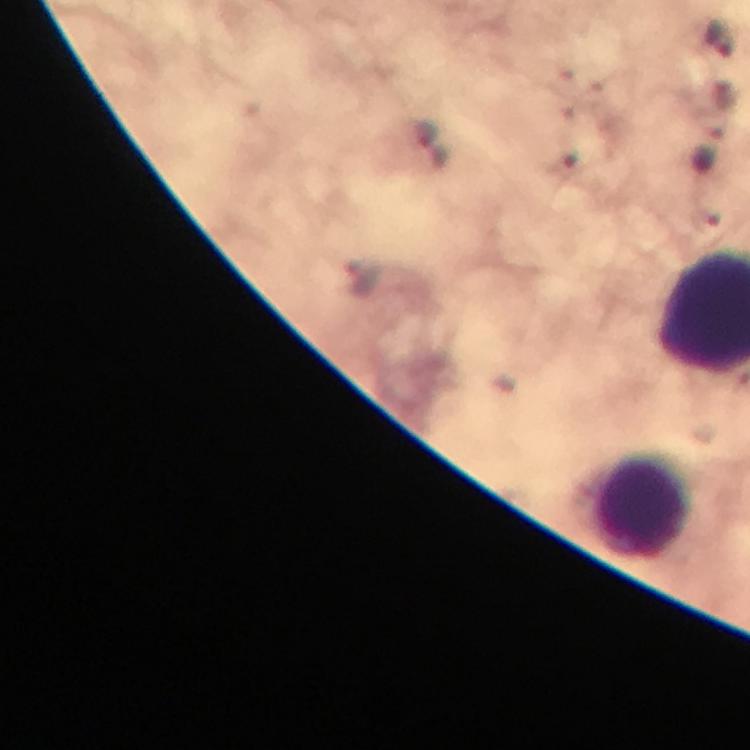

Approximate object centers, in pixels from the top-left corner.
Summary:
  - Plasmodium parasite locations: (x=434, y=147)
  - Leukocyte locations: (x=640, y=508)
  - Immersion oil: used
  - Cropped from: a single field of view
  - Magnification: 100x
  - Context: from a diagnostic examination for malaria
  - Capture: smartphone mounted on the microscope
  - Image size: 750×750 pixels
  - Preparation: thick blood film
  - Stain: Giemsa